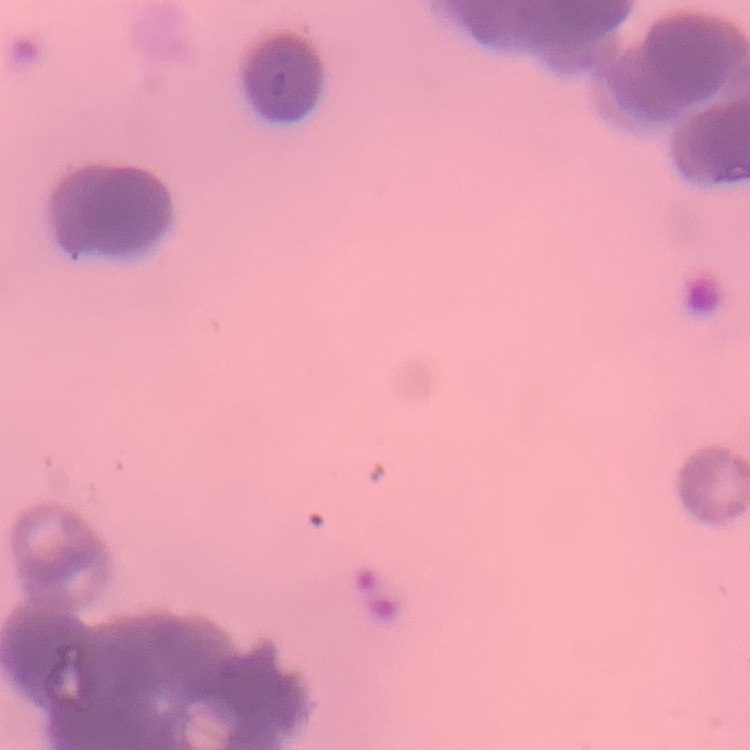

Summary:
  - Red blood cell morphology: rouleaux formation
  - Preparation: thin blood film
  - Stain: Field's or Giemsa
  - Image type: one tile cut from a larger photomicrograph